Name the parasite shown.
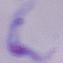

This is a trypanosome.

{
  "modality": "micrograph",
  "magnification": "1000x"
}